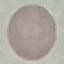
malaria status = uninfected
capture = smartphone through the microscope eyepiece
image type = automatically extracted cell patch, resized to 64 × 64 pixels
stain = Giemsa
preparation = thin blood smear